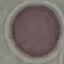
malaria_status: uninfected
stain: Giemsa
capture: smartphone through the microscope eyepiece
image_type: cell patch, automatically extracted from a larger field of view and resized to 64 × 64 pixels
preparation: thin smear